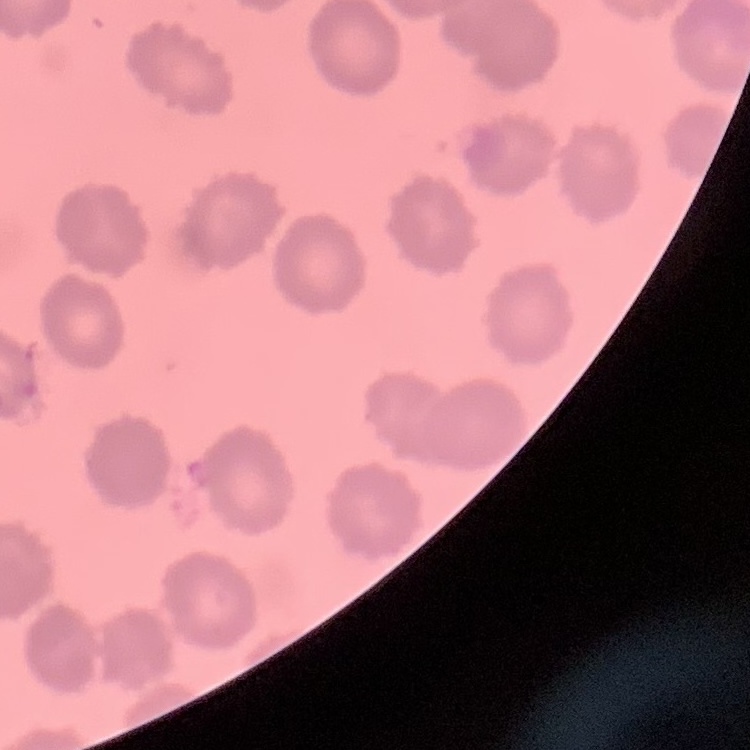

Summary:
  - Red blood cell morphology: no rouleaux formation
  - Image type: square crop of a larger photomicrograph
  - Stain: Field's or Giemsa
  - Preparation: thin peripheral smear